Identify the parasite.
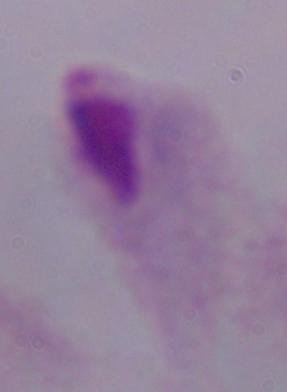

This is a trichomonad.

Photomicrograph. 1000x magnification.